Identify the preparation type.
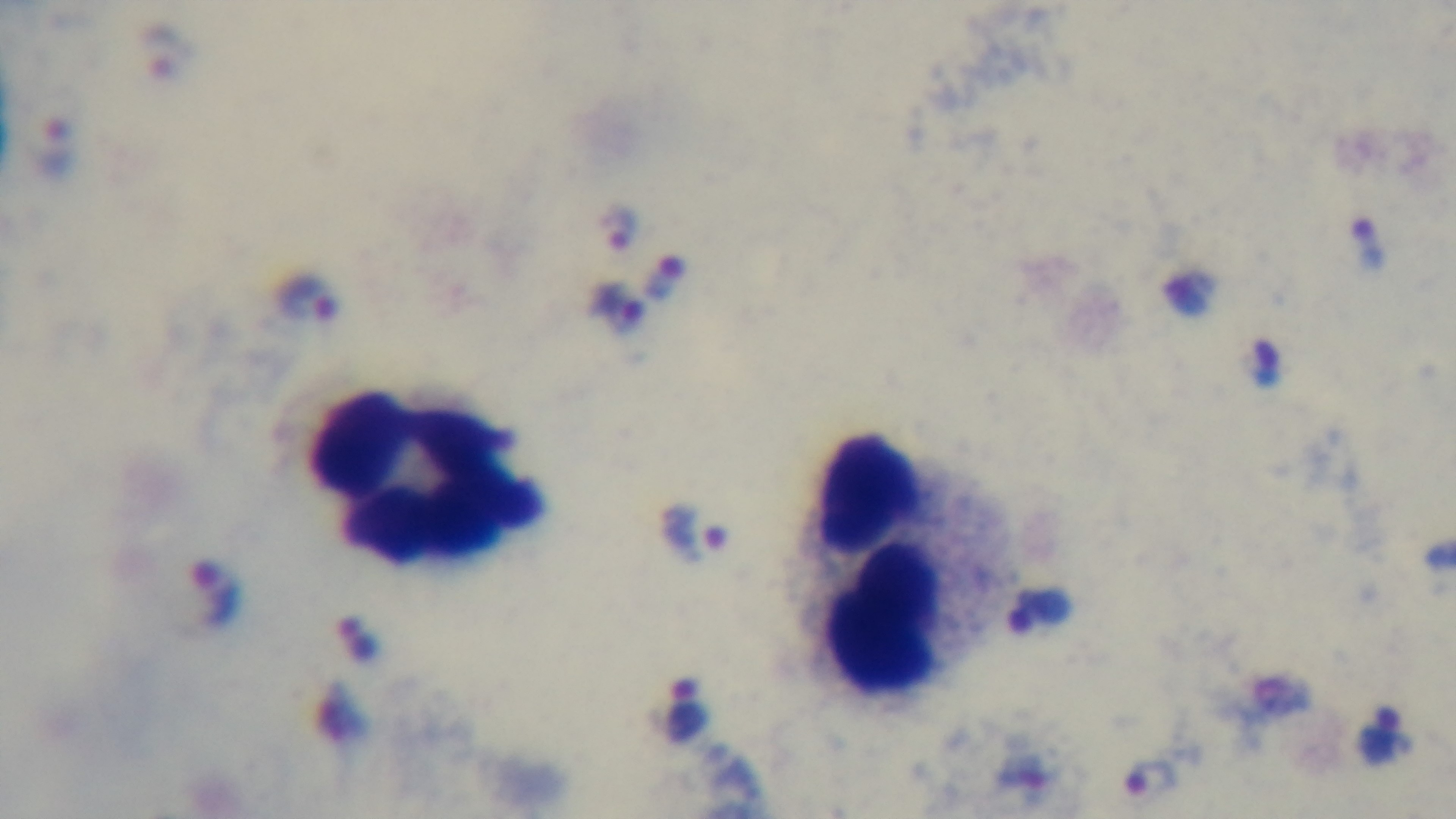

A thick smear.

Giemsa stain. Light microscopy. 100x oil-immersion objective. Malaria status: infected. Single field of view. Captured with a mounted 4K digital camera.